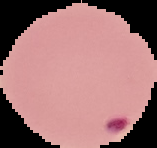
Summary:
  - Image size: 157×148 pixels
  - Malaria status: parasitized
  - Image type: cell region segmented out of the field of view; surrounding area masked to black
  - Preparation: thin blood smear